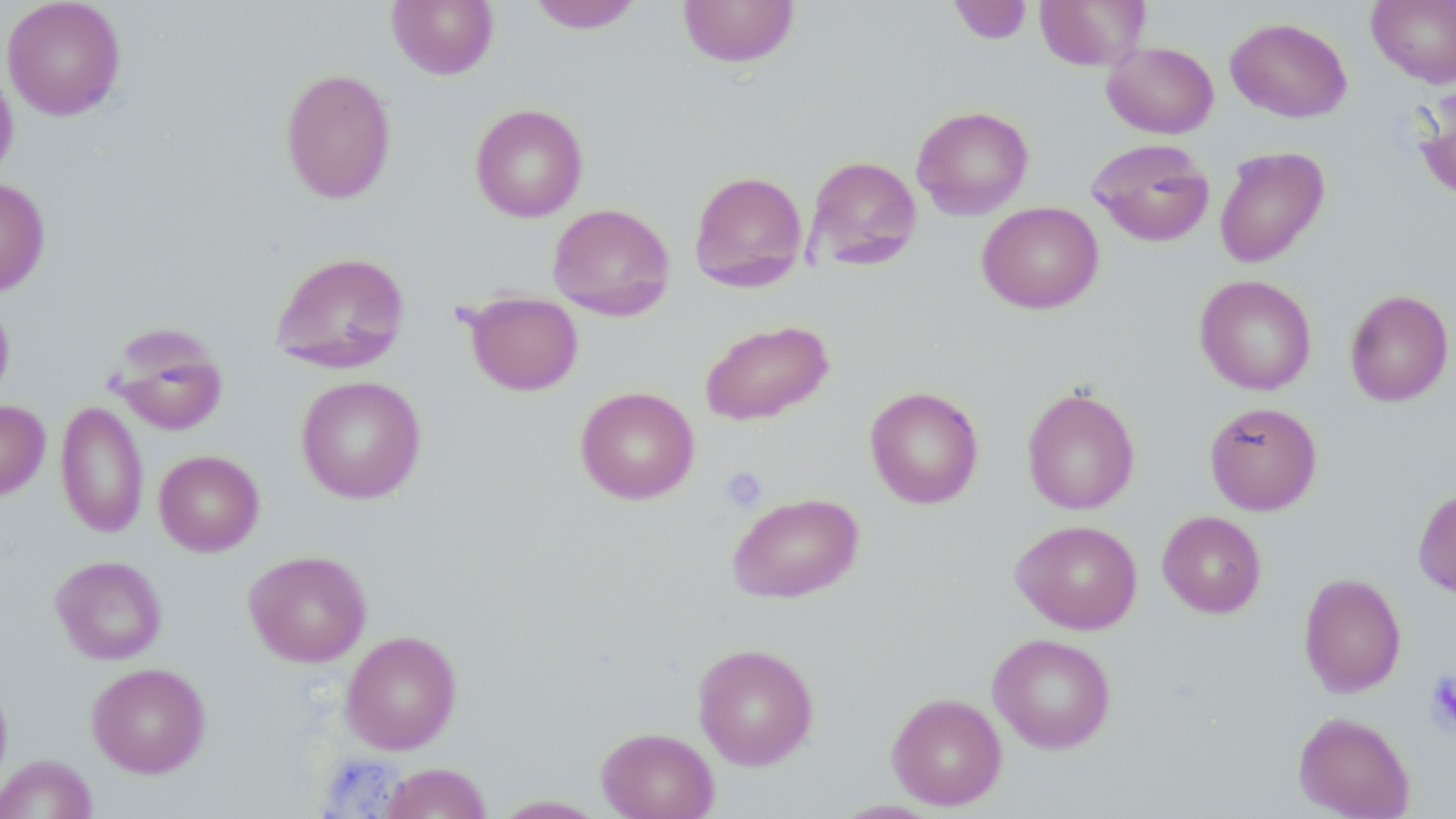
Summary:
  - Coordinate format: approximate bounding boxes as [x1, y1, x2, y2] in pixels
  - Uninfected red blood cell locations: [2, 0, 126, 120], [386, 0, 500, 80], [677, 0, 801, 68], [1034, 0, 1151, 70], [1366, 0, 1456, 88], [526, 1, 644, 33], [947, 1, 1033, 45], [1224, 17, 1353, 123], [1101, 42, 1219, 139], [0, 59, 18, 184], [279, 67, 397, 204], [1413, 84, 1456, 204], [469, 103, 588, 223], [911, 105, 1034, 220], [1087, 138, 1215, 247], [1213, 146, 1330, 268], [802, 155, 923, 273], [688, 170, 808, 292], [0, 177, 50, 298], [977, 201, 1104, 315], [547, 203, 675, 321], [269, 251, 411, 375], [1195, 275, 1317, 396], [1344, 288, 1454, 406], [463, 291, 583, 397], [0, 296, 15, 406], [699, 319, 834, 426], [108, 326, 229, 436], [295, 376, 427, 504], [574, 386, 701, 505], [864, 386, 984, 509], [1022, 386, 1140, 515], [0, 400, 50, 500], [55, 400, 149, 538], [1204, 401, 1322, 515], [154, 450, 264, 556], [1413, 486, 1456, 599], [727, 492, 864, 603], [1157, 511, 1267, 618], [1010, 519, 1142, 634], [244, 550, 372, 667], [50, 555, 167, 665], [1298, 572, 1407, 698], [341, 630, 462, 755], [987, 633, 1116, 753], [692, 643, 819, 770], [86, 662, 210, 778], [0, 674, 13, 797], [886, 692, 1007, 810], [1292, 711, 1415, 818], [596, 726, 719, 819], [0, 754, 98, 819], [378, 762, 491, 819], [490, 795, 610, 818]
  - Platelet locations: [720, 465, 769, 514], [1426, 669, 1456, 734]
  - Slide-level diagnosis: no evidence of blood parasites
  - Preparation: thin blood film
  - Magnification: 1000x
  - Field of view: single
  - Image size: 1456×819 pixels
  - Stain: May-Grünwald-Giemsa
  - Modality: light microscopy